Classify this cell by malaria status.
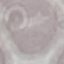

Uninfected.

Summary:
  - Capture: smartphone camera at the microscope eyepiece
  - Stain: Giemsa
  - Preparation: thin blood film
  - Image type: cell patch, automatically extracted from a larger field of view and resized to 64 × 64 pixels